Point out each Plasmodium parasite.
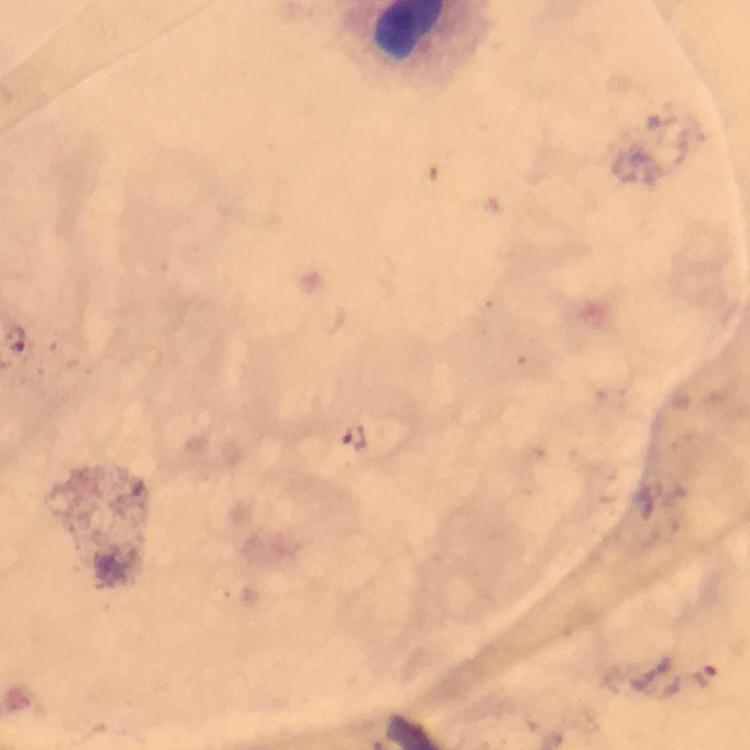
Approximate centers as (x, y) in pixels.
Plasmodium parasites: (16, 339), (356, 438).

Cropped region of a single field of view. From a malaria diagnostic workup. Thick smear. Giemsa stain. Photographed through the microscope with a smartphone camera. 100x magnification. Immersion oil applied. Image is 750×750 pixels.